Classify this cell by malaria status.
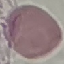
It is uninfected.

preparation: thin blood smear
stain: Giemsa
image_type: cell patch, automatically extracted from a larger field of view and resized to 64 × 64 pixels
capture: smartphone camera at the microscope eyepiece